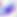
Captured at 400x magnification. Toxoplasma gondii is shown. Photomicrograph.